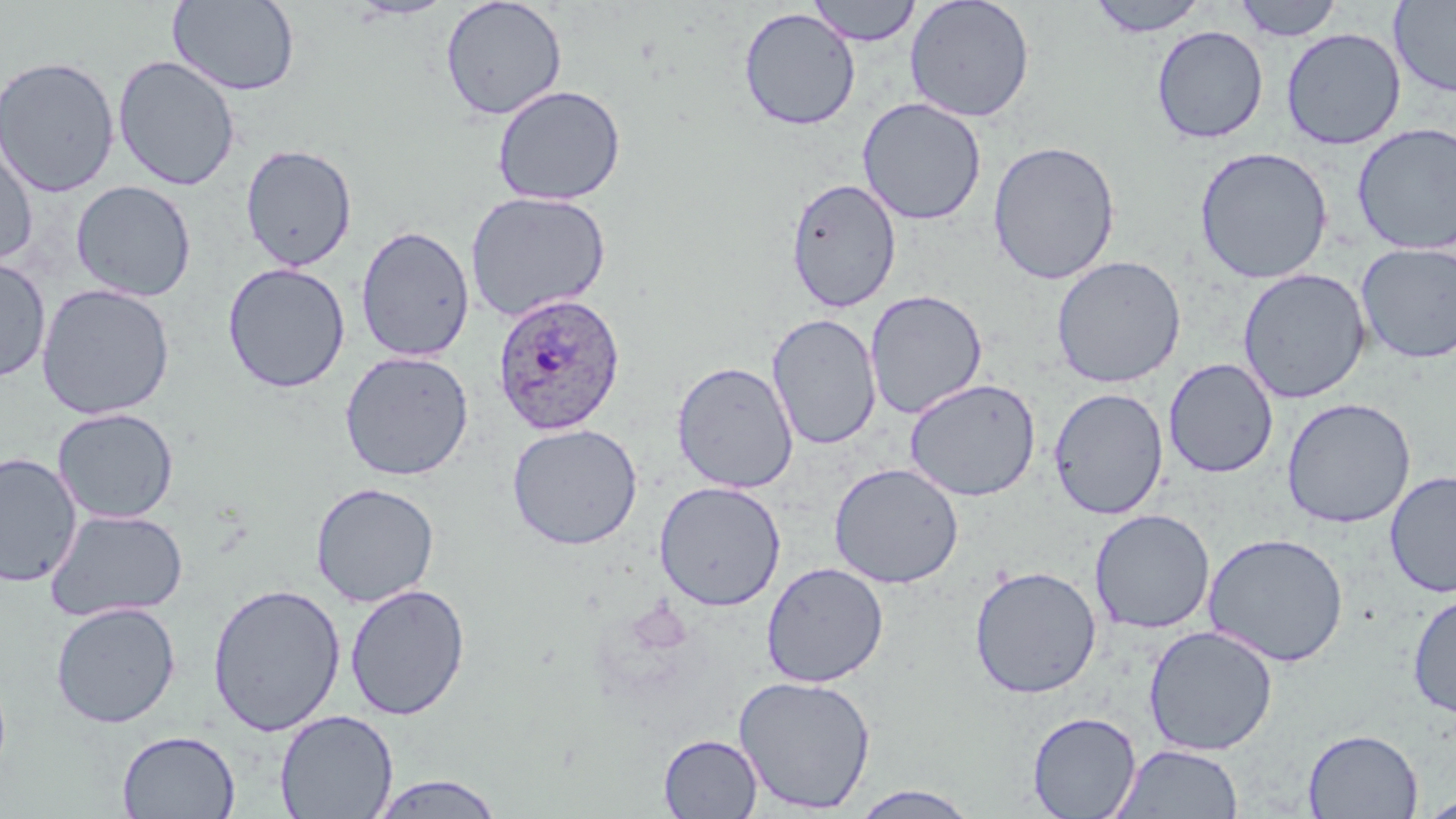 Approximate bounding boxes as (x1, y1, x2, y2) in pixels. Plasmodium ovale-infected red blood cell locations: (492, 292, 627, 435). Uninfected red blood cell locations: (346, 0, 456, 20), (807, 0, 922, 46), (904, 0, 1035, 123), (1085, 0, 1211, 37), (1231, 0, 1344, 41), (1389, 0, 1456, 98), (167, 1, 301, 96), (440, 1, 567, 121), (738, 7, 861, 131), (1151, 25, 1269, 144), (1281, 27, 1406, 150), (0, 55, 120, 198), (112, 55, 241, 191), (492, 84, 626, 206), (857, 97, 987, 225), (1351, 122, 1456, 256), (0, 138, 38, 267), (988, 140, 1121, 285), (241, 143, 357, 272), (1194, 146, 1333, 284), (786, 177, 901, 313), (71, 180, 197, 301), (465, 190, 612, 322), (355, 225, 475, 362), (1355, 243, 1456, 363), (1259, 253, 1456, 375), (1051, 255, 1187, 388), (0, 257, 51, 383), (222, 262, 350, 394), (1237, 268, 1371, 404), (36, 284, 175, 419), (865, 290, 987, 419), (767, 313, 882, 450), (339, 350, 474, 481), (1163, 358, 1279, 478), (671, 360, 799, 493), (906, 378, 1041, 502), (1048, 387, 1169, 520), (1281, 397, 1416, 528), (52, 407, 179, 523), (506, 422, 643, 550), (0, 452, 83, 589), (828, 462, 964, 588), (1385, 470, 1456, 597), (654, 480, 786, 611), (310, 482, 440, 607), (44, 509, 188, 622), (1089, 509, 1215, 634), (1203, 532, 1349, 667), (761, 561, 889, 688), (968, 565, 1102, 699), (207, 582, 346, 736), (344, 583, 471, 720), (1407, 591, 1456, 719), (50, 602, 181, 728), (1143, 625, 1278, 756), (734, 674, 876, 814), (274, 709, 398, 819), (1027, 711, 1141, 819), (1302, 728, 1423, 818), (116, 730, 240, 818), (659, 734, 763, 818), (1111, 743, 1245, 818), (367, 773, 506, 818), (848, 785, 981, 818), (1418, 795, 1456, 818). Slide-level diagnosis: Plasmodium ovale. Single field of view. May-Grünwald-Giemsa-stained preparation. Image is 1456×819 pixels. Thin blood smear. Light microscopy. 1000x magnification.